Give the position of every Plasmodium parasite and every leukocyte.
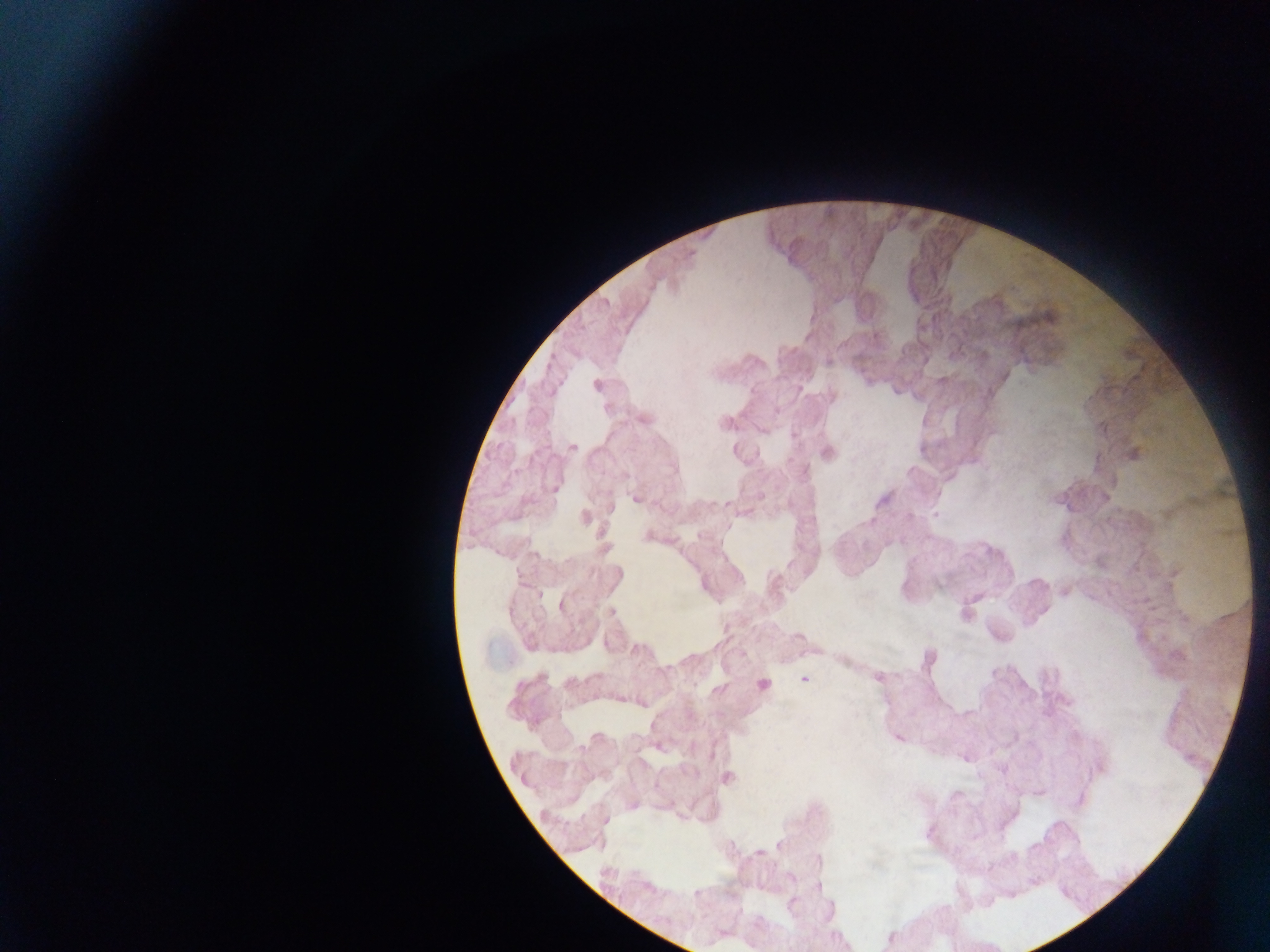
Approximate centers as {x, y} in pixels.
Plasmodium parasites (some below the resolvable threshold): {803, 679}.
No leukocytes observed.

Sample from Ghana. Mobile-phone photograph taken through the microscope. Image is 1270×952 pixels. One field of view. Thick blood film.